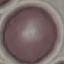

Result: no malaria parasites seen. Automatically extracted cell patch, resized to 64 × 64 pixels. Thin blood smear. Photographed with a smartphone camera at the microscope eyepiece. Giemsa stain.